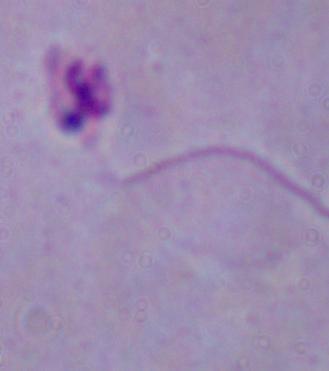
1000x magnification. A Leishmania parasite is seen. Micrograph.